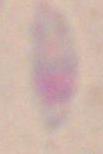

Summary:
  - Modality: micrograph
  - Magnification: 1000x
  - Identification: Toxoplasma gondii